Locate every Plasmodium falciparum-infected red blood cell.
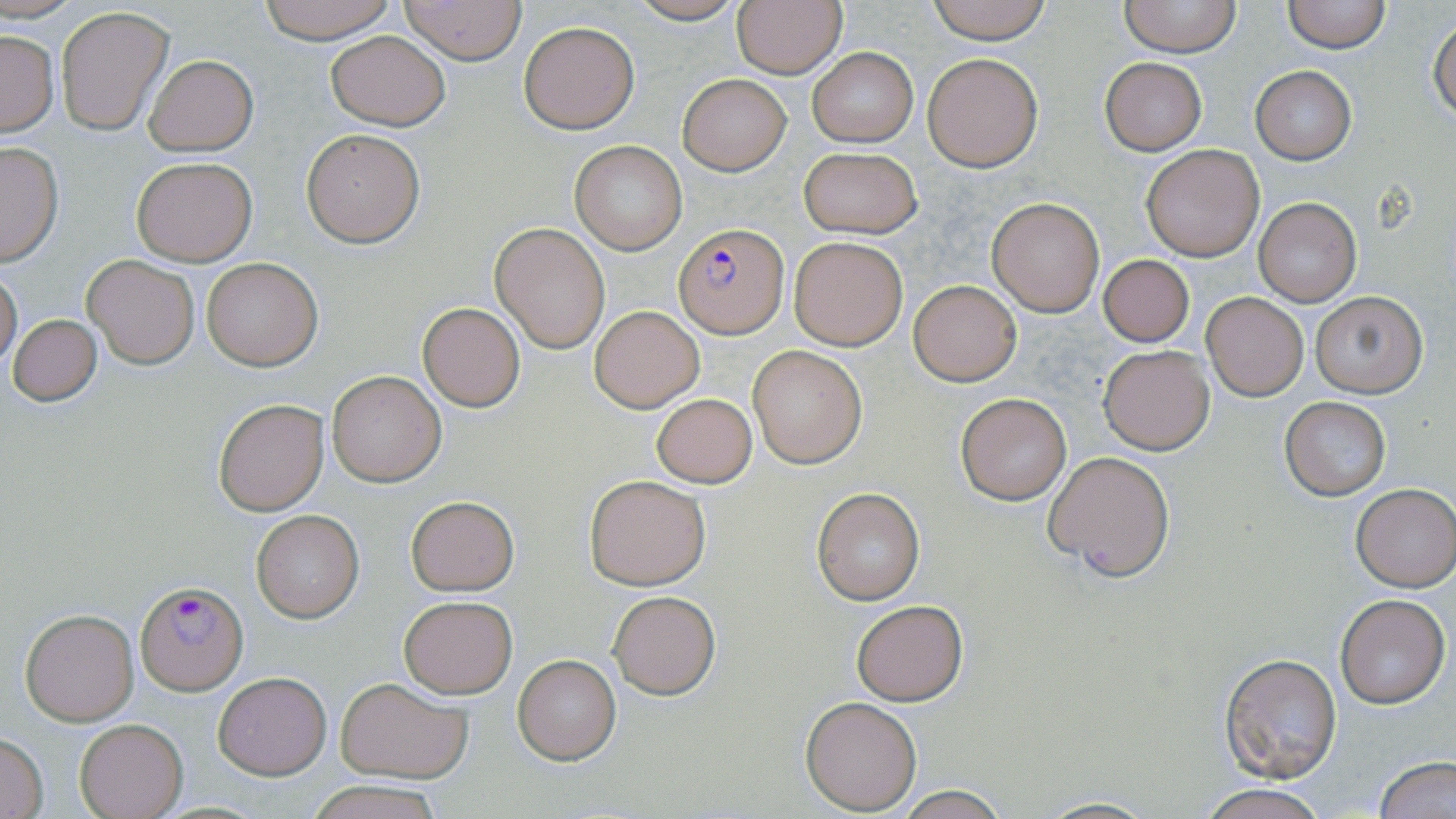
Approximate bounding boxes as [x1, y1, x2, y2] in pixels.
Plasmodium falciparum-infected red blood cells: [677, 224, 787, 337], [135, 581, 245, 693].

{
  "slide_level_diagnosis": "Plasmodium falciparum",
  "stain": "May-Grünwald-Giemsa",
  "magnification": "1000x",
  "image_size": "1456×819 pixels",
  "uninfected_red_blood_cell_locations": "approximate bounding boxes as [x1, y1, x2, y2] in pixels: [254, 0, 400, 42], [400, 0, 527, 65], [623, 0, 748, 24], [731, 0, 846, 79], [923, 0, 1056, 45], [1120, 0, 1243, 57], [1281, 0, 1391, 53], [56, 5, 174, 136], [1429, 17, 1455, 122], [517, 21, 639, 134], [0, 29, 58, 135], [325, 32, 451, 130], [807, 48, 917, 147], [923, 53, 1043, 172], [145, 55, 257, 155], [1101, 58, 1206, 155], [1250, 66, 1357, 163], [677, 73, 792, 175], [300, 128, 425, 246], [568, 139, 687, 256], [0, 141, 63, 266], [1140, 144, 1264, 261], [797, 147, 923, 237], [131, 156, 255, 264], [987, 196, 1107, 317], [1252, 196, 1362, 307], [490, 221, 610, 354], [789, 236, 907, 350], [82, 254, 200, 369], [1097, 254, 1194, 346], [200, 255, 323, 371], [0, 267, 22, 369], [908, 280, 1022, 386], [1310, 290, 1429, 400], [1201, 292, 1307, 401], [418, 302, 526, 413], [589, 305, 704, 412], [7, 314, 101, 406], [1098, 344, 1216, 455], [748, 345, 866, 468], [327, 371, 445, 485], [955, 392, 1073, 506], [650, 393, 757, 488], [1279, 396, 1390, 500], [212, 398, 329, 516], [1044, 451, 1176, 581], [582, 474, 710, 590], [1351, 483, 1456, 591], [811, 487, 926, 605], [405, 495, 520, 596], [250, 509, 364, 623], [607, 591, 721, 699], [1334, 593, 1450, 708], [398, 596, 517, 699], [850, 600, 968, 705], [20, 608, 138, 726], [1218, 650, 1344, 783], [512, 654, 621, 764], [213, 672, 331, 779], [336, 675, 475, 782], [801, 696, 921, 815], [76, 718, 187, 819], [0, 733, 49, 818], [1376, 756, 1455, 819], [303, 781, 447, 819], [1195, 782, 1330, 819], [1033, 796, 1163, 818]",
  "modality": "light microscopy",
  "field_of_view": "single",
  "preparation": "thin blood smear"
}